Classify this cell by malaria status.
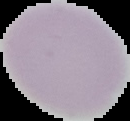

Uninfected.

Cell region segmented out of the field of view; the surrounding area is masked to black. From a thin blood smear. Image is 130×121 pixels.